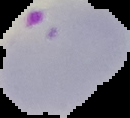

Summary:
  - Image type: cell region segmented out of the field of view; surrounding area masked to black
  - Result: Plasmodium parasites identified
  - Preparation: thin blood film
  - Image size: 130×118 pixels